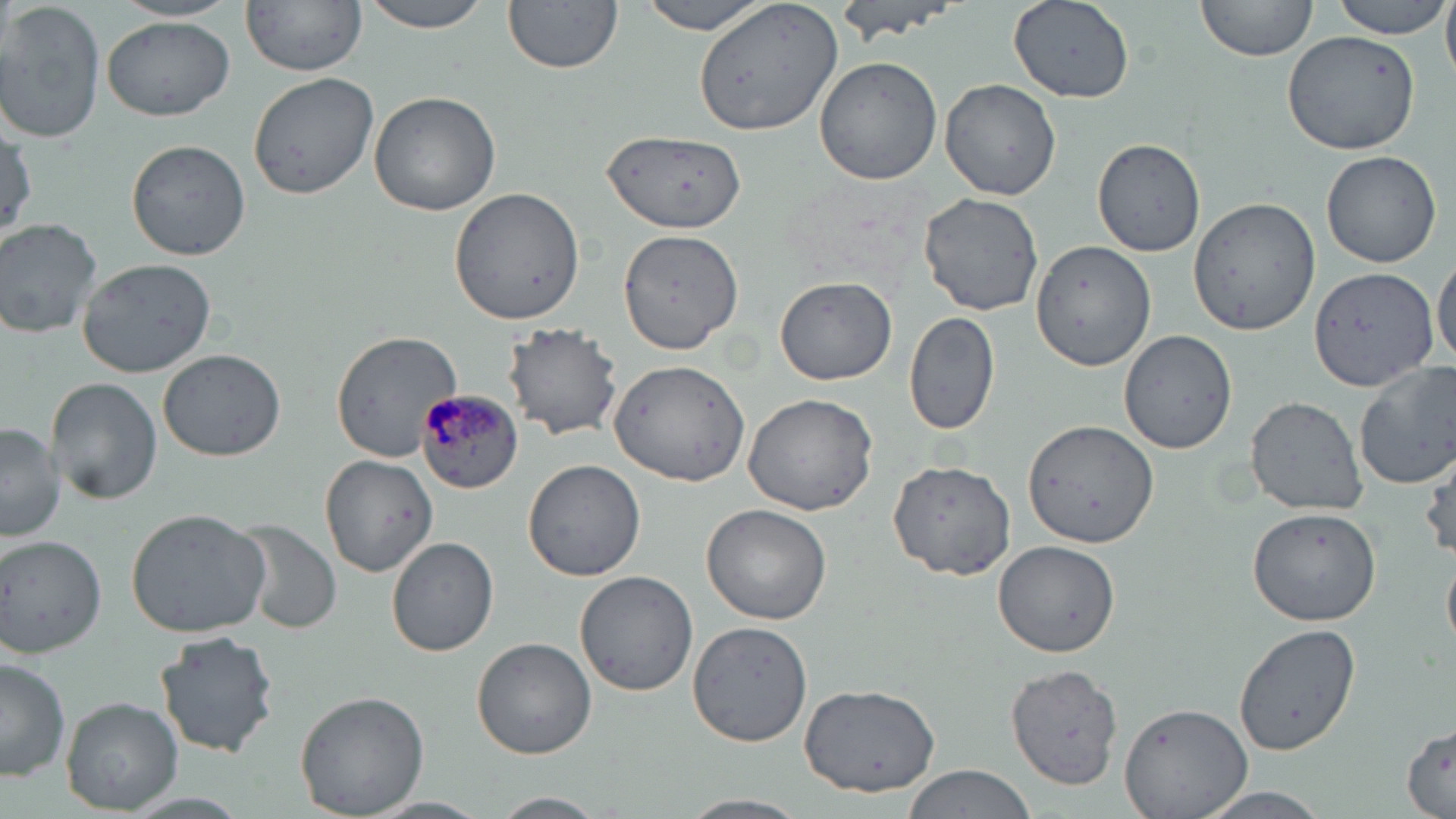

slide_level_diagnosis: Plasmodium malariae
magnification: 1000x
plasmodium_malariae_infected_red_blood_cell_locations: 'approximate bounding boxes as (x1,y1)-(x2,y2) corner pairs in pixels: (416,389)-(524,496)'
uninfected_red_blood_cell_locations: 'approximate bounding boxes as (x1,y1)-(x2,y2) corner pairs in pixels: (0,0)-(107,145), (109,0)-(240,23), (241,0)-(369,75), (359,0)-(493,33), (502,0)-(621,74), (637,0)-(779,35), (693,0)-(843,138), (833,0)-(962,43), (1008,0)-(1134,101), (1194,0)-(1318,61), (1333,0)-(1450,38), (1442,0)-(1456,81), (101,17)-(234,121), (1281,27)-(1423,157), (814,57)-(942,185), (247,71)-(378,200), (940,79)-(1061,201), (368,91)-(500,216), (0,121)-(38,241), (603,130)-(745,234), (1092,137)-(1208,256), (126,140)-(252,260), (1321,149)-(1442,267), (449,184)-(585,323), (918,192)-(1045,317), (1188,197)-(1320,336), (0,217)-(102,337), (619,228)-(742,355), (1029,240)-(1157,371), (1431,252)-(1455,369), (75,257)-(218,377), (1309,266)-(1439,390), (774,275)-(896,385), (903,311)-(1001,438), (503,322)-(625,440), (1118,329)-(1238,454), (329,330)-(460,462), (157,348)-(286,461), (609,357)-(753,485), (1353,360)-(1456,489), (44,378)-(162,505), (742,393)-(878,516), (1245,396)-(1368,515), (0,421)-(64,543), (1022,421)-(1160,551), (319,452)-(439,577), (887,458)-(1017,580), (522,459)-(646,582), (702,502)-(834,625), (1247,506)-(1383,627), (125,507)-(272,638), (233,518)-(342,632), (386,536)-(499,657), (0,537)-(108,657), (992,539)-(1123,658), (1443,549)-(1456,655), (575,571)-(699,696), (1234,620)-(1359,757), (686,621)-(815,749), (154,630)-(282,757), (471,635)-(598,758), (1,658)-(71,782), (1005,663)-(1124,793), (799,683)-(940,796), (294,689)-(428,817), (62,696)-(182,814), (1120,700)-(1254,819), (1401,721)-(1454,815), (902,762)-(1041,819), (1194,788)-(1335,819), (490,792)-(607,818), (682,792)-(806,819), (368,796)-(490,818)'
stain: May-Grünwald-Giemsa
modality: light microscopy
field_of_view: one of a larger specimen
preparation: thin blood film
image_size: 1456×819 pixels